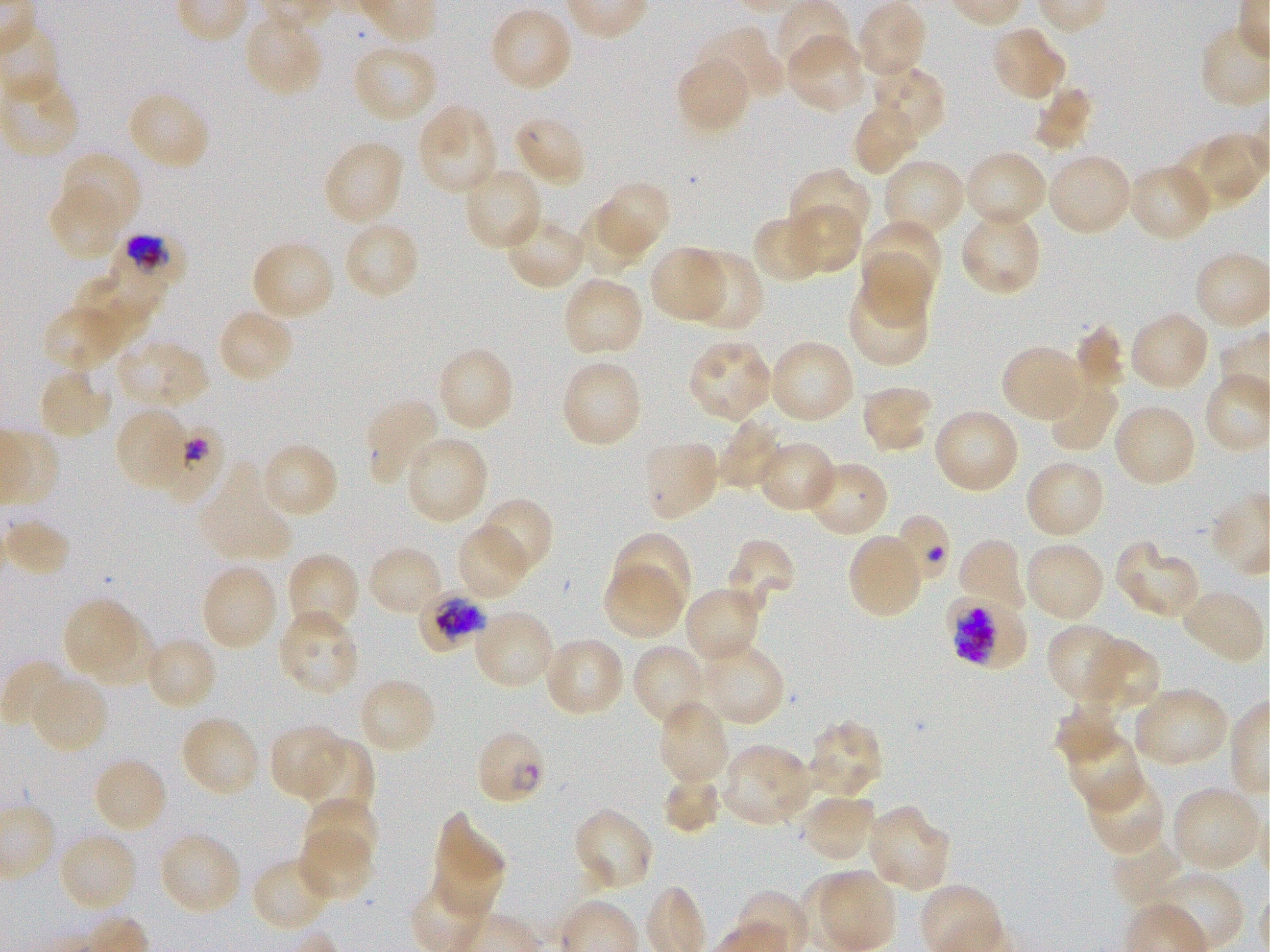

Approximate bounding boxes as {x1, y1, x2, y2} in pixels. Not every red blood cell is marked. A life-cycle stage — or a range of stages, where the recorded stages span more than one — follows each staged infected red blood cell.
Summary:
  - Locations of uninfected red blood cells: {775, 2, 853, 76}, {855, 3, 927, 80}, {488, 7, 574, 93}, {243, 14, 325, 97}, {697, 26, 783, 102}, {990, 26, 1067, 102}, {786, 34, 867, 114}, {351, 44, 438, 123}, {676, 56, 752, 135}, {871, 66, 947, 143}, {0, 76, 81, 160}, {1033, 86, 1092, 152}, {126, 90, 212, 171}, {851, 102, 921, 177}, {416, 103, 498, 195}, {512, 114, 587, 189}, {1176, 137, 1262, 211}, {322, 140, 405, 227}, {963, 150, 1049, 230}, {61, 151, 142, 233}, {1047, 152, 1133, 237}, {882, 158, 966, 239}, {1127, 162, 1213, 243}, {462, 166, 544, 252}, {788, 167, 872, 246}, {595, 181, 671, 256}, {48, 186, 123, 260}, {788, 202, 861, 275}, {576, 205, 655, 279}, {959, 209, 1043, 298}, {752, 214, 824, 285}, {505, 216, 588, 290}, {861, 220, 943, 295}, {343, 221, 421, 302}, {250, 239, 336, 321}, {648, 246, 726, 323}, {860, 250, 932, 331}, {686, 251, 765, 334}, {92, 266, 170, 318}, {562, 275, 645, 358}, {77, 278, 149, 347}, {847, 281, 930, 368}, {43, 304, 123, 373}, {217, 308, 295, 384}, {1128, 310, 1211, 392}, {1074, 324, 1126, 392}, {116, 338, 210, 411}, {685, 338, 774, 422}, {768, 338, 856, 425}, {436, 346, 516, 432}, {1001, 346, 1086, 425}, {560, 358, 643, 449}, {37, 370, 114, 441}, {1047, 381, 1119, 453}, {859, 384, 934, 453}, {364, 396, 442, 486}, {1113, 403, 1197, 488}, {931, 407, 1021, 494}, {114, 408, 189, 492}, {717, 415, 785, 492}, {403, 434, 489, 526}, {640, 438, 720, 521}, {758, 440, 839, 514}, {260, 441, 341, 521}, {805, 459, 890, 538}, {1024, 459, 1106, 539}, {198, 463, 293, 563}, {479, 496, 555, 577}, {2, 518, 72, 577}, {457, 523, 527, 601}, {611, 531, 691, 612}, {847, 533, 924, 619}, {956, 537, 1025, 611}, {725, 539, 796, 611}, {1023, 541, 1106, 622}, {1115, 543, 1202, 619}, {367, 544, 443, 619}, {284, 552, 360, 637}, {200, 563, 279, 652}, {603, 564, 683, 639}, {683, 585, 763, 665}, {1180, 589, 1267, 666}, {62, 598, 138, 673}, {276, 609, 361, 697}, {472, 610, 554, 690}, {85, 616, 160, 689}, {1046, 623, 1130, 703}, {143, 636, 219, 712}, {543, 637, 626, 718}, {1086, 637, 1160, 711}, {631, 642, 707, 728}, {695, 643, 786, 728}, {2, 660, 73, 734}, {27, 674, 109, 755}, {357, 676, 437, 756}, {1132, 686, 1231, 768}, {657, 700, 731, 786}, {1054, 701, 1122, 766}, {179, 714, 261, 797}, {806, 718, 884, 799}, {268, 724, 346, 800}, {1065, 731, 1145, 812}, {301, 739, 375, 819}, {718, 743, 813, 828}, {92, 756, 169, 834}, {1086, 772, 1165, 856}, {662, 774, 723, 834}, {1171, 784, 1260, 873}, {800, 793, 878, 863}, {302, 795, 379, 871}, {866, 805, 951, 893}, {573, 808, 655, 894}, {432, 814, 505, 921}, {58, 830, 139, 913}, {298, 830, 373, 900}, {158, 831, 242, 916}, {1109, 837, 1184, 908}, {251, 855, 334, 932}, {1146, 869, 1245, 951}, {815, 872, 896, 949}
  - Locations of infected red blood cells: {110, 236, 189, 285} trophozoite; {157, 419, 227, 506}; {418, 589, 491, 654} early trophozoite to early schizont; {946, 590, 1027, 670} late trophozoite to early schizont; {475, 728, 546, 807}
  - Field of view: one from this slide
  - Image size: 1270×952 pixels
  - Donor blood group: O+
  - Preparation: thin blood smear
  - Objective: 100x, oil immersion, numerical aperture 1.25
  - Stain: Giemsa
  - Culture: P. falciparum strain 3D7, static, in vitro